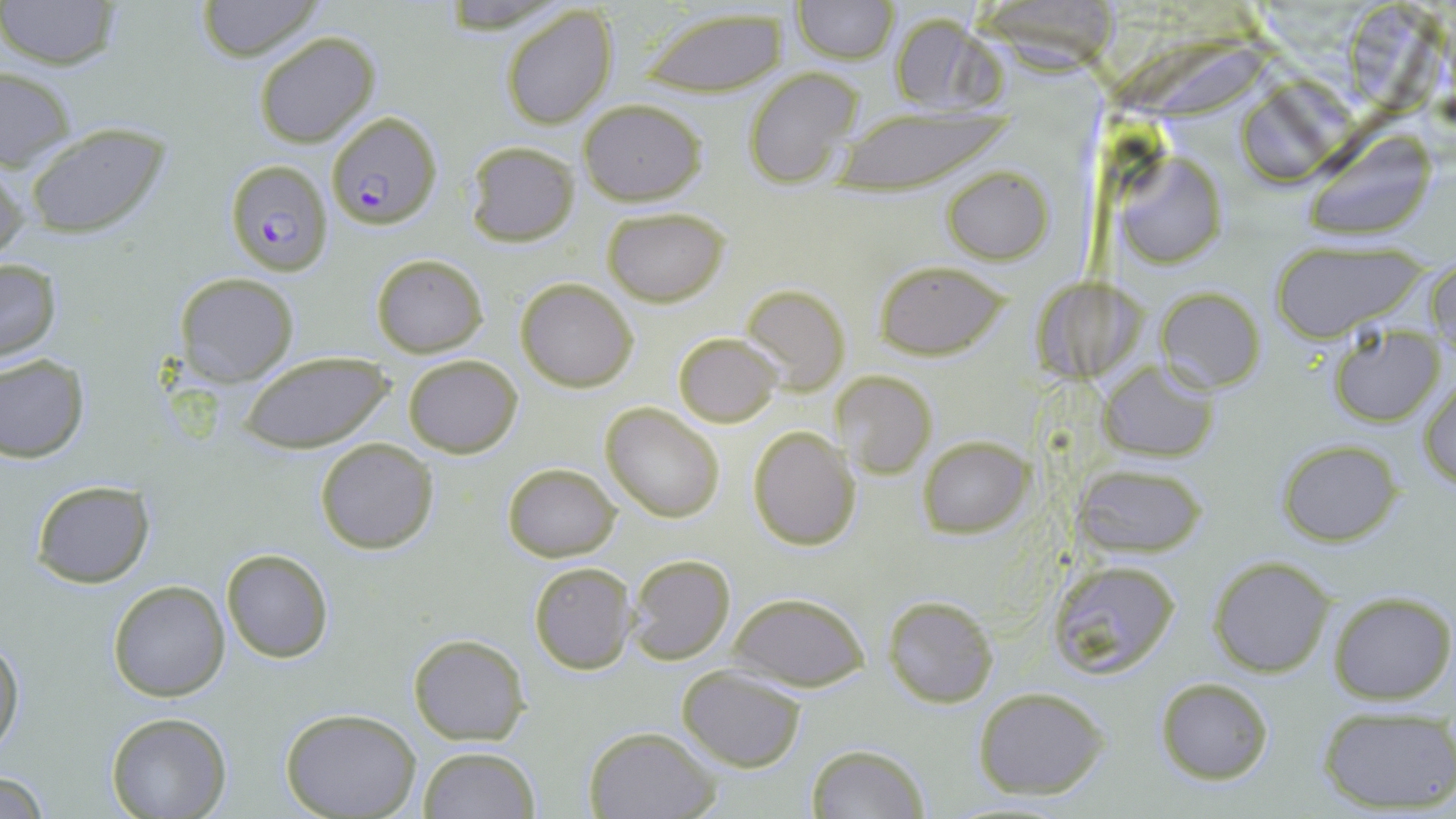
Approximate bounding boxes as (x1,y1)-(x2,y2) corner pairs in pixels. Uninfected red blood cell locations: (0,0)-(124,72), (194,0)-(324,61), (791,1)-(897,63), (499,5)-(618,130), (638,5)-(791,98), (887,10)-(1007,118), (253,30)-(379,146), (0,63)-(75,173), (744,67)-(864,189), (1235,81)-(1343,189), (578,100)-(707,206), (830,107)-(1006,191), (23,123)-(171,239), (1302,130)-(1440,243), (465,141)-(580,246), (1117,157)-(1228,270), (0,158)-(28,270), (942,166)-(1052,263), (602,206)-(730,307), (1269,241)-(1430,341), (371,252)-(489,358), (1429,255)-(1456,361), (0,256)-(63,361), (874,259)-(1012,361), (175,273)-(300,387), (515,277)-(638,392), (742,284)-(849,396), (1156,287)-(1265,392), (1329,325)-(1446,428), (674,331)-(783,427), (239,352)-(389,454), (0,354)-(91,462), (404,354)-(522,457), (1099,360)-(1219,462), (835,371)-(935,480), (1419,377)-(1455,491), (601,402)-(724,521), (749,425)-(862,551), (918,434)-(1035,538), (315,438)-(440,554), (1276,439)-(1402,545), (1073,461)-(1209,559), (502,463)-(620,562), (30,479)-(156,588), (222,548)-(335,663), (627,553)-(737,667), (1209,556)-(1335,677), (1045,559)-(1182,681), (529,563)-(637,674), (109,581)-(229,701), (1329,590)-(1455,704), (728,591)-(871,693), (883,595)-(998,707), (408,634)-(529,745), (0,636)-(24,760), (676,666)-(806,770), (1155,677)-(1273,784), (971,686)-(1112,799), (1318,705)-(1454,813), (282,709)-(422,819), (106,712)-(232,819), (583,726)-(719,819), (806,744)-(929,818), (418,745)-(541,818), (2,772)-(52,818). Plasmodium falciparum-infected red blood cell locations: (327,112)-(441,229), (228,159)-(334,275). Slide-level diagnosis: Plasmodium falciparum. Single field of view. 1000x magnification. May-Grünwald-Giemsa stain. Image is 1456×819 pixels. Optical microscopy. Thin blood film.